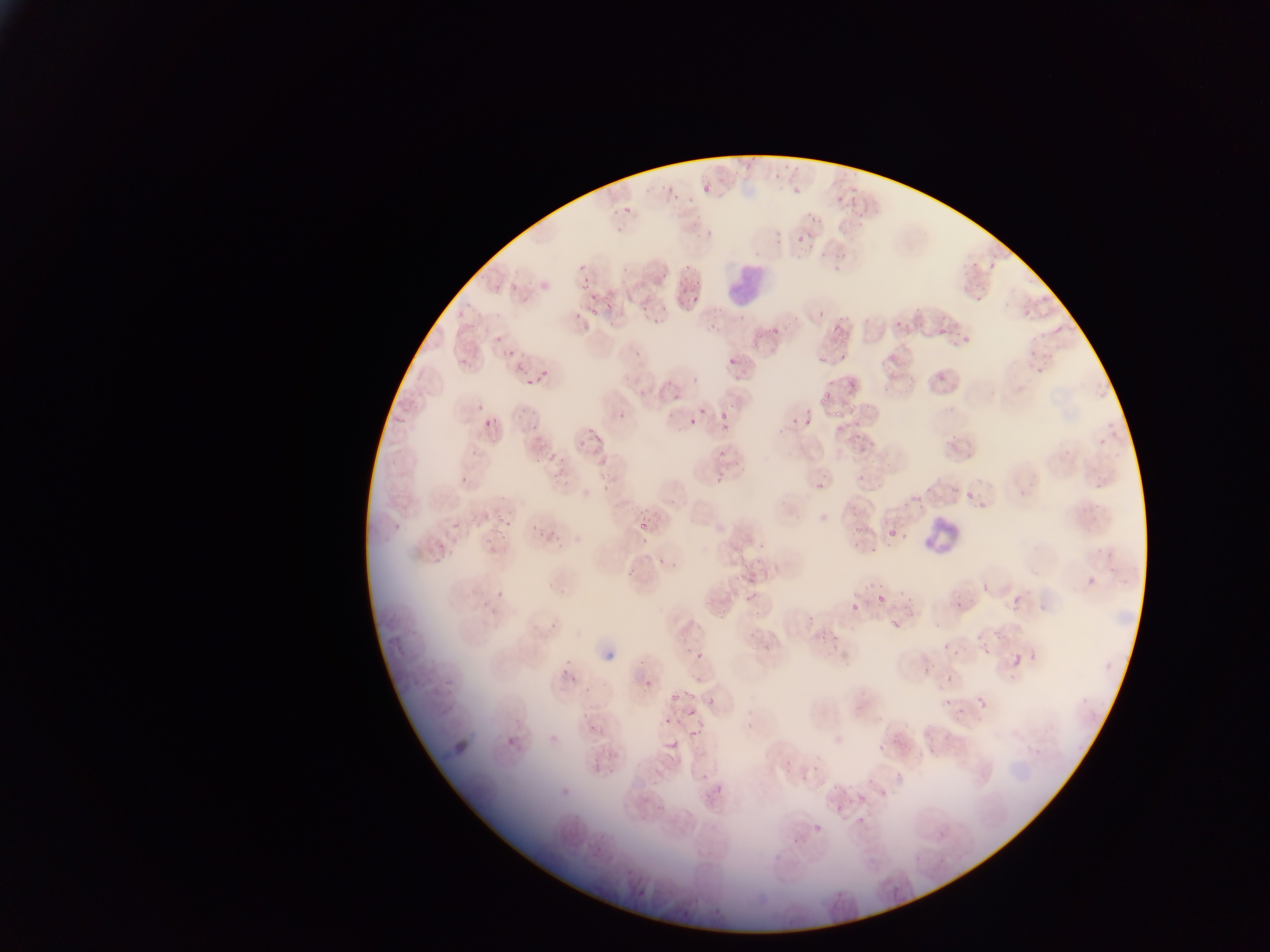
capture = mobile-phone photograph through a microscope
country = Ghana
field of view = single
malaria parasite locations = approximate bounding boxes as left top right bottom in pixels: 700 172 719 193; 661 176 687 198; 789 183 806 198; 850 187 864 211; 822 190 844 210; 619 203 635 216; 834 212 855 236; 806 215 824 223; 792 220 802 245; 818 250 828 263; 835 255 853 261; 983 258 996 273; 486 272 511 299; 682 274 702 296; 509 276 522 292; 580 277 591 289; 973 281 994 304; 580 286 616 318; 639 295 664 317; 1023 297 1041 317; 891 305 918 329; 459 316 483 335; 765 321 776 339; 828 324 838 341; 1055 324 1064 333; 840 326 855 357; 938 327 947 335; 954 332 978 347; 1026 332 1041 350; 724 337 748 368; 628 339 649 361; 894 340 909 355; 501 342 522 359; 455 346 477 368; 816 351 832 366; 1023 357 1051 382; 524 361 551 393; 935 368 953 387; 842 374 853 391; 681 379 697 385; 825 379 835 390; 670 384 693 405; 819 393 830 408; 469 398 491 416; 716 404 734 419; 831 405 843 425; 702 407 710 416; 527 408 549 425; 483 417 496 428; 804 417 812 427; 688 418 698 427; 787 418 800 428; 1093 421 1127 447; 714 424 726 435; 835 424 847 437; 944 426 965 451; 585 428 604 454; 712 450 729 458; 596 454 614 472; 549 459 567 476; 709 463 731 489; 458 473 470 484; 856 475 865 484; 816 481 825 490; 925 482 935 492; 967 485 987 505; 845 497 863 514; 455 502 482 537; 487 507 513 534; 632 510 659 532; 530 515 555 542; 753 520 764 554; 850 529 860 536; 887 530 896 539; 735 546 751 566; 655 550 683 574; 624 563 639 578; 1080 565 1107 594; 980 572 995 596; 862 574 882 594; 744 579 762 608; 481 588 497 612; 899 588 915 608; 711 591 730 623; 878 595 886 603; 949 596 961 614; 1006 597 1016 612; 852 604 859 612; 884 614 902 632; 807 615 816 624; 983 647 991 655; 692 652 702 660; 558 653 576 678; 1011 654 1022 667; 946 676 952 684; 642 679 652 692; 668 679 679 701; 687 689 697 702; 941 695 955 710; 977 696 986 705; 707 698 715 706; 683 703 701 719; 656 712 675 726; 921 723 943 752; 741 724 756 736; 584 726 624 777; 689 730 697 739; 872 731 893 753; 666 733 680 750; 549 734 559 744; 505 737 515 747; 801 768 816 781; 707 776 738 798; 881 788 889 797; 858 793 867 802; 653 797 669 810; 832 800 843 818; 851 814 870 831; 812 817 830 834; 933 830 943 840; 885 876 903 903 | approximate x y pixel centers of objects too small to bound: 946 646
leukocyte locations = approximate bounding boxes as left top right bottom in pixels: 728 249 794 310; 914 505 961 564
image size = 1270×952 pixels
preparation = thin blood film